Comment on the morphology of the red blood cells.
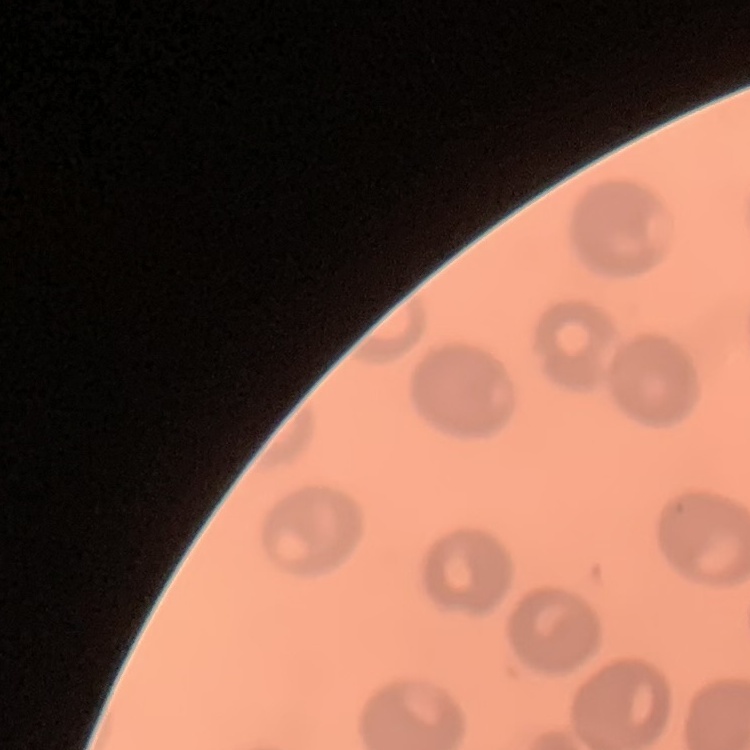

No rouleaux formation.

preparation = thin blood smear
stain = Field's or Giemsa
image type = square crop of a larger photomicrograph